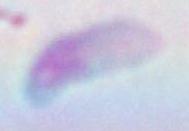 Captured at 1000x magnification. Micrograph. Toxoplasma gondii is seen.